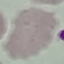

Malaria status: uninfected. Acquired by smartphone through the microscope eyepiece. Giemsa stain. Cell patch, automatically extracted from a larger field of view and resized to 64 × 64 pixels. Thin smear of blood.